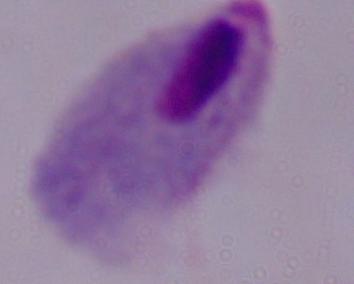
{
  "identification": "trichomonad",
  "magnification": "1000x",
  "modality": "micrograph"
}